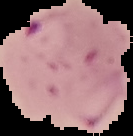

Cell region segmented out of the field of view; the surrounding area is masked to black. Result: malaria parasites detected. Image is 133×136 pixels. From a thin blood film.